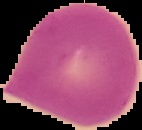
image type = segmented cell region with the area outside set to black
malaria status = uninfected
image size = 142×130 pixels
preparation = thin blood smear